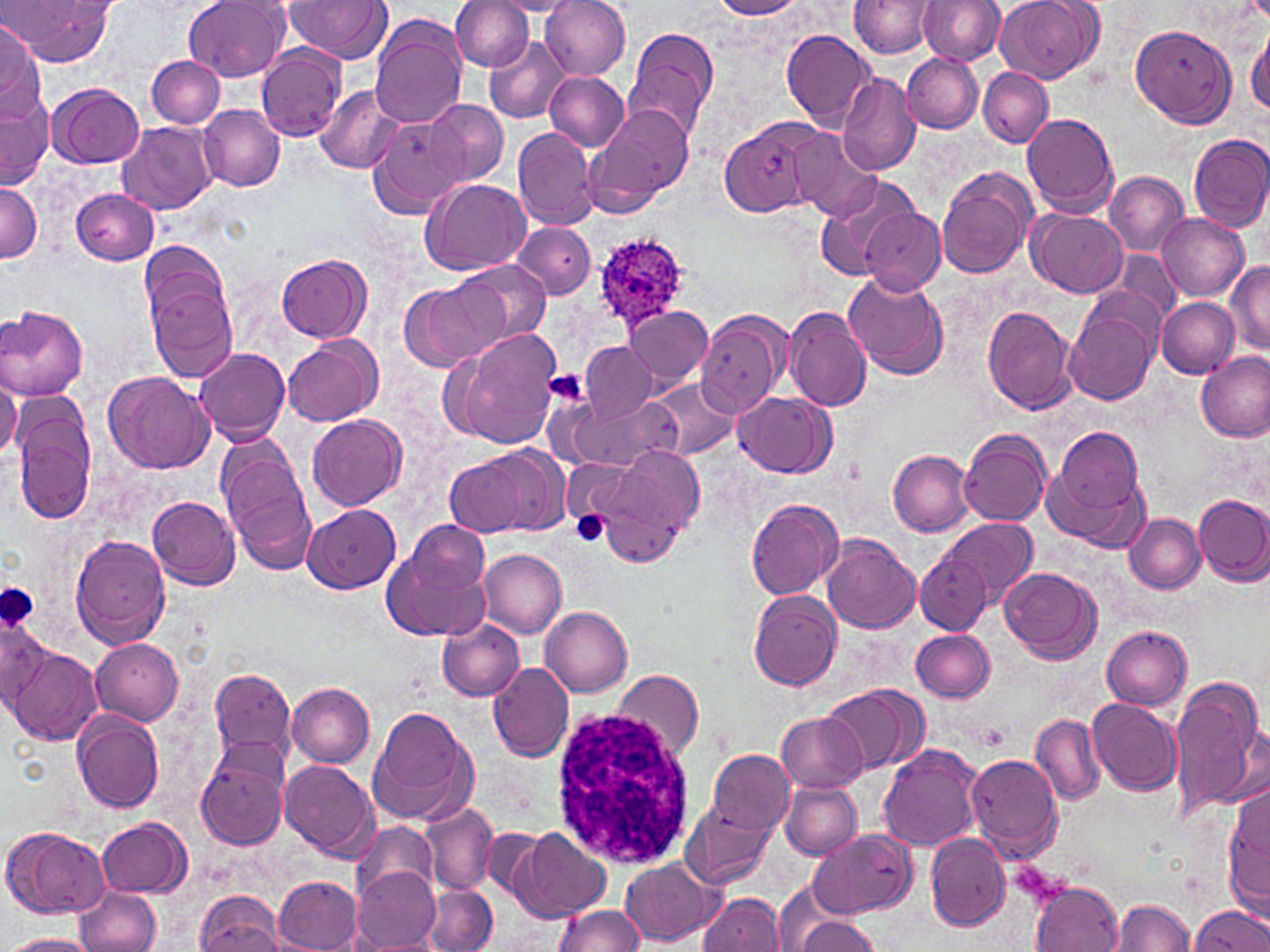 Approximate bounding boxes as [x1, y1, x2, y2] in pixels. Platelet locations: [547, 370, 588, 404], [572, 511, 611, 547], [0, 582, 42, 635], [979, 723, 1010, 750]. Plasmodium ovale-infected red blood cell locations: [589, 232, 690, 330]. White blood cell locations: [550, 705, 700, 871]. Uninfected red blood cell locations: [6, 0, 115, 68], [184, 0, 289, 81], [452, 0, 535, 72], [540, 0, 630, 80], [711, 0, 802, 19], [849, 0, 939, 58], [917, 0, 1003, 65], [994, 0, 1102, 83], [285, 1, 389, 62], [491, 1, 581, 16], [371, 17, 467, 128], [1130, 22, 1236, 128], [0, 25, 42, 121], [1247, 25, 1270, 122], [624, 26, 719, 144], [782, 30, 879, 132], [485, 37, 569, 123], [255, 46, 347, 142], [901, 53, 983, 133], [146, 55, 224, 128], [978, 67, 1052, 148], [544, 72, 628, 150], [836, 73, 921, 176], [48, 81, 143, 168], [317, 86, 403, 175], [1, 90, 52, 188], [425, 99, 508, 186], [585, 101, 695, 214], [200, 105, 285, 192], [1023, 113, 1118, 217], [366, 116, 465, 218], [717, 117, 824, 217], [118, 121, 218, 214], [513, 128, 599, 230], [787, 128, 882, 221], [1188, 133, 1270, 233], [935, 167, 1037, 279], [1105, 172, 1188, 255], [814, 177, 921, 281], [419, 178, 529, 276], [0, 183, 41, 262], [72, 189, 159, 264], [858, 206, 943, 295], [1025, 207, 1128, 299], [1157, 213, 1249, 301], [514, 221, 594, 299], [139, 241, 228, 329], [1115, 251, 1181, 323], [277, 253, 371, 342], [451, 259, 551, 347], [1227, 261, 1270, 355], [841, 271, 949, 379], [146, 279, 239, 380], [402, 280, 498, 370], [1157, 298, 1240, 377], [1064, 301, 1159, 405], [0, 305, 88, 401], [783, 305, 873, 412], [625, 306, 712, 390], [982, 306, 1077, 414], [696, 311, 790, 415], [445, 331, 564, 450], [284, 335, 383, 426], [583, 341, 658, 422], [196, 347, 291, 444], [1195, 352, 1270, 442], [104, 371, 214, 474], [0, 375, 20, 459], [647, 379, 740, 461], [734, 391, 835, 479], [569, 395, 675, 470], [11, 400, 96, 523], [308, 414, 406, 513], [1043, 427, 1149, 550], [960, 429, 1052, 528], [216, 440, 315, 571], [444, 445, 567, 540], [603, 447, 703, 558], [888, 450, 976, 535], [564, 460, 633, 523], [1194, 493, 1270, 584], [148, 495, 241, 589], [746, 498, 844, 600], [302, 505, 400, 594], [1125, 514, 1206, 592], [940, 517, 1036, 607], [408, 520, 490, 594], [71, 534, 170, 648], [821, 536, 919, 634], [382, 542, 491, 642], [478, 548, 566, 639], [915, 551, 990, 634], [999, 566, 1102, 663], [748, 591, 843, 691], [541, 606, 632, 697], [1, 616, 56, 713], [437, 618, 526, 702], [1102, 626, 1192, 710], [912, 630, 994, 701], [91, 637, 183, 724], [7, 643, 103, 746], [487, 660, 574, 764], [210, 666, 296, 762], [613, 669, 703, 762], [1169, 676, 1267, 820], [286, 683, 375, 767], [823, 684, 927, 777], [1089, 699, 1183, 799], [368, 709, 476, 825], [73, 711, 165, 813], [777, 713, 867, 792], [1031, 713, 1102, 804], [195, 740, 291, 850], [878, 745, 983, 854], [708, 750, 795, 835], [966, 752, 1064, 861], [280, 760, 380, 860], [780, 781, 861, 859], [1226, 785, 1270, 912], [683, 801, 773, 889], [417, 804, 496, 895], [98, 817, 191, 897], [353, 822, 436, 900], [3, 827, 111, 919], [483, 827, 548, 901], [511, 827, 610, 921], [809, 830, 918, 917], [925, 834, 1009, 931], [619, 858, 720, 945], [353, 866, 441, 950], [274, 874, 362, 952], [771, 879, 851, 951], [1030, 882, 1123, 952], [75, 886, 161, 952], [424, 886, 497, 952], [195, 891, 287, 952], [699, 892, 787, 950], [1109, 898, 1194, 951], [1190, 904, 1269, 951], [553, 905, 646, 951], [791, 916, 880, 952], [3, 935, 99, 952]. Slide-level diagnosis: Plasmodium ovale. 1000x magnification. Image is 1270×952 pixels. Optical microscopy. May-Grünwald-Giemsa-stained preparation. Thin blood smear. One field of a larger specimen.